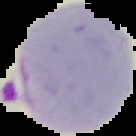
preparation = thin blood film
malaria status = parasitized
image type = segmented cell region with the area outside set to black
image size = 136×136 pixels